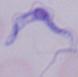
modality = micrograph
identification = trypanosome
magnification = 1000x